Identify the parasite.
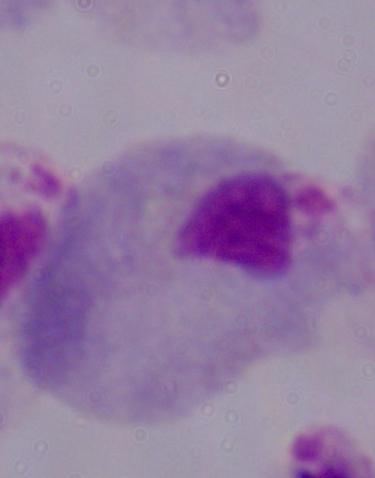
A trichomonad.

Photomicrograph. Captured at 1000x magnification.